Find each parasitized red blood cell.
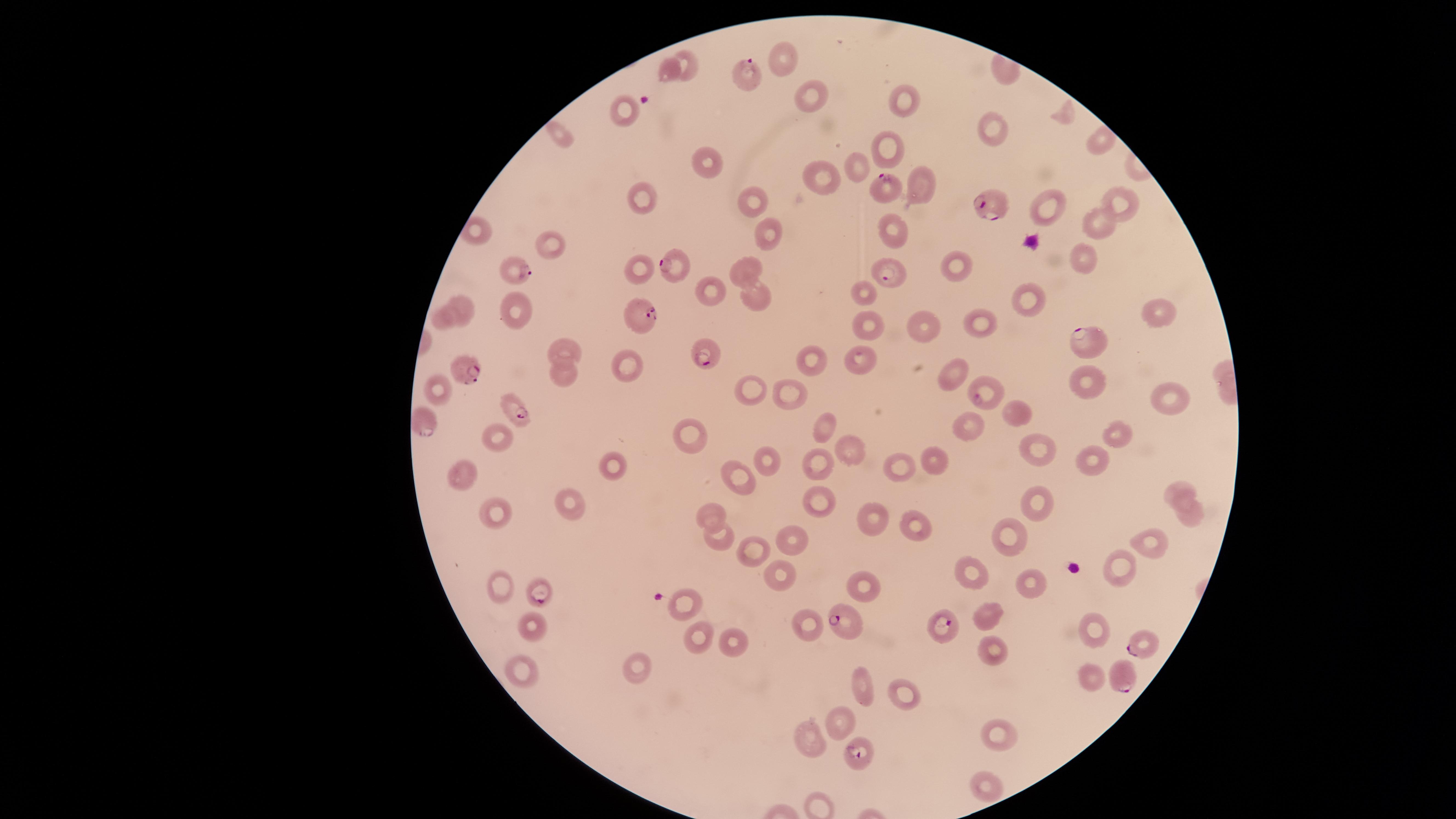
Approximate marker points, in pixels from the top-left corner.
Parasitized red blood cells: (x=742, y=66), (x=885, y=183), (x=995, y=200), (x=669, y=260), (x=513, y=269), (x=887, y=273), (x=637, y=315), (x=1089, y=338), (x=703, y=354), (x=462, y=363), (x=986, y=392), (x=511, y=401), (x=423, y=416), (x=539, y=590), (x=845, y=618), (x=944, y=628), (x=1137, y=642), (x=1121, y=679), (x=859, y=751).

{
  "capture": "smartphone photograph through the microscope eyepiece",
  "image_size": "1456×819 pixels",
  "uninfected_red_blood_cells": "approximate marker points, in pixels from the top-left corner: (x=786, y=53), (x=689, y=58), (x=667, y=69), (x=813, y=96), (x=909, y=100), (x=621, y=111), (x=990, y=122), (x=565, y=135), (x=1103, y=140), (x=891, y=148), (x=706, y=158), (x=855, y=165), (x=823, y=177), (x=924, y=189), (x=643, y=197), (x=751, y=199), (x=1117, y=199), (x=1049, y=210), (x=478, y=224), (x=1098, y=224), (x=892, y=231), (x=768, y=235), (x=556, y=244), (x=1080, y=257), (x=952, y=264), (x=638, y=267), (x=746, y=274), (x=714, y=291), (x=866, y=291), (x=758, y=298), (x=463, y=302), (x=1028, y=302), (x=516, y=309), (x=1159, y=312), (x=443, y=316), (x=981, y=317), (x=867, y=325), (x=923, y=325), (x=556, y=348), (x=812, y=354), (x=631, y=358), (x=859, y=365), (x=952, y=372), (x=564, y=374), (x=1076, y=382), (x=436, y=386), (x=740, y=392), (x=784, y=393), (x=1165, y=397), (x=1015, y=418), (x=969, y=425), (x=824, y=426), (x=684, y=429), (x=1124, y=433), (x=498, y=438), (x=1040, y=447), (x=850, y=449), (x=929, y=459), (x=1093, y=460), (x=769, y=461), (x=612, y=464), (x=820, y=466), (x=899, y=468), (x=465, y=474), (x=733, y=479), (x=1179, y=482), (x=820, y=496), (x=1039, y=501), (x=573, y=503), (x=708, y=512), (x=493, y=513), (x=876, y=513), (x=1188, y=513), (x=914, y=523), (x=715, y=535), (x=1001, y=535), (x=791, y=540), (x=1150, y=542), (x=754, y=553), (x=1117, y=568), (x=974, y=570), (x=778, y=577), (x=1025, y=579), (x=497, y=581), (x=862, y=585), (x=683, y=603), (x=991, y=609), (x=810, y=619), (x=1092, y=626), (x=530, y=628), (x=698, y=639), (x=737, y=643), (x=991, y=647), (x=635, y=666), (x=519, y=672), (x=1091, y=673), (x=867, y=683), (x=900, y=693), (x=840, y=721), (x=994, y=731), (x=806, y=736), (x=979, y=781)",
  "visible_region": "circular",
  "species": "Plasmodium falciparum",
  "stain": "Giemsa",
  "field_of_view": "single",
  "preparation": "thin blood film"
}